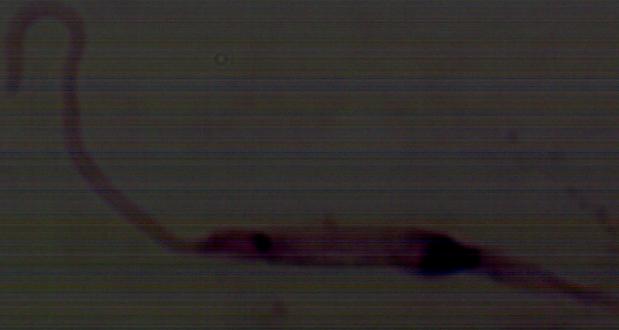
Summary:
  - Modality: photomicrograph
  - Identification: Leishmania
  - Magnification: 1000x